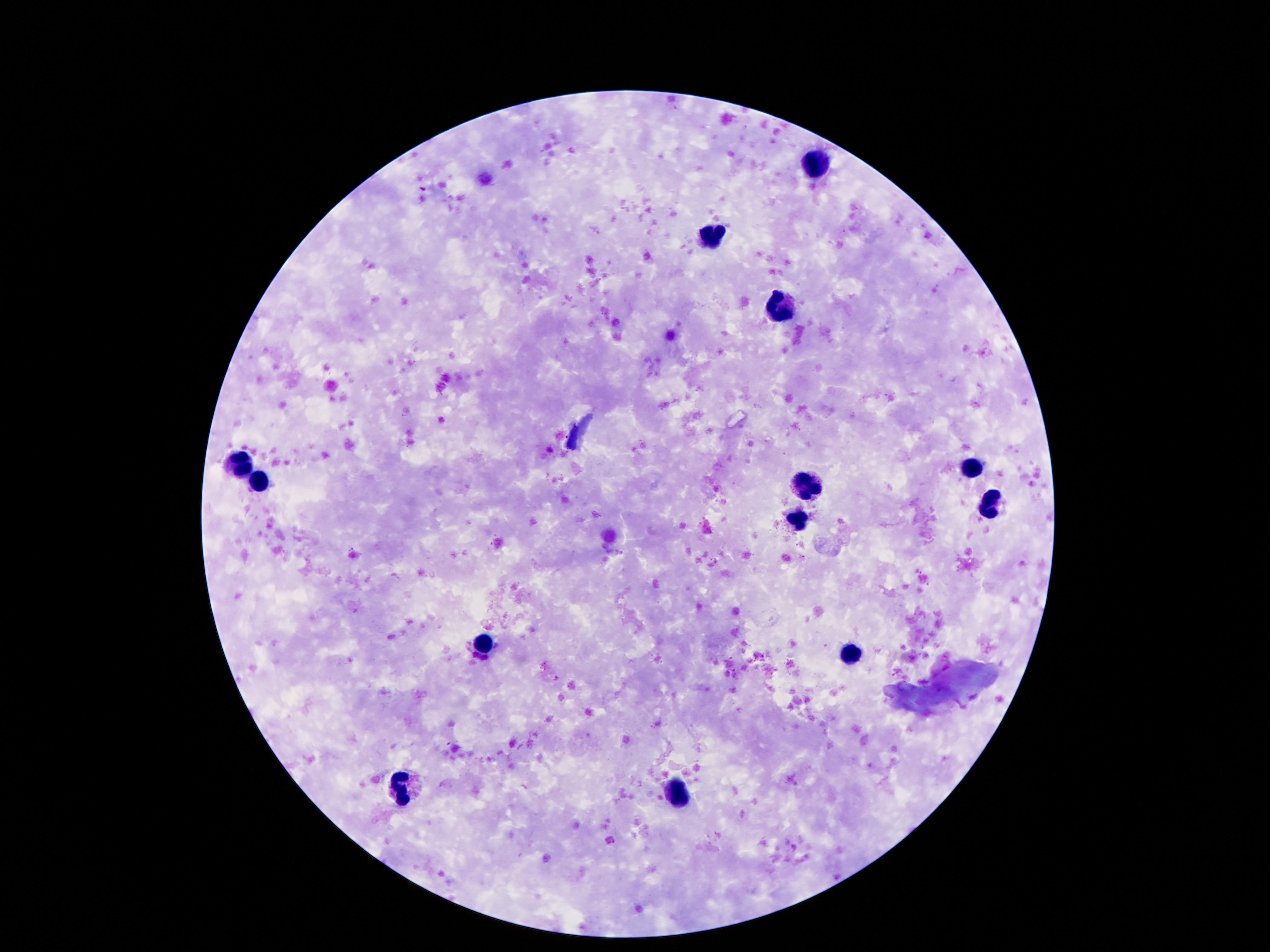 Approximate object centers, in pixels from the top-left corner. Leukocyte locations: (x=816, y=165), (x=708, y=232), (x=777, y=305), (x=972, y=468), (x=241, y=470), (x=261, y=482), (x=804, y=484), (x=988, y=503), (x=798, y=521), (x=485, y=643), (x=849, y=654), (x=403, y=787), (x=681, y=790). Smartphone photograph taken through the microscope eyepiece. Patient malaria status: not infected. Giemsa stain. Thick blood smear. 100x magnification. One field from this slide. Image is 1270×952 pixels.